State the preparation type.
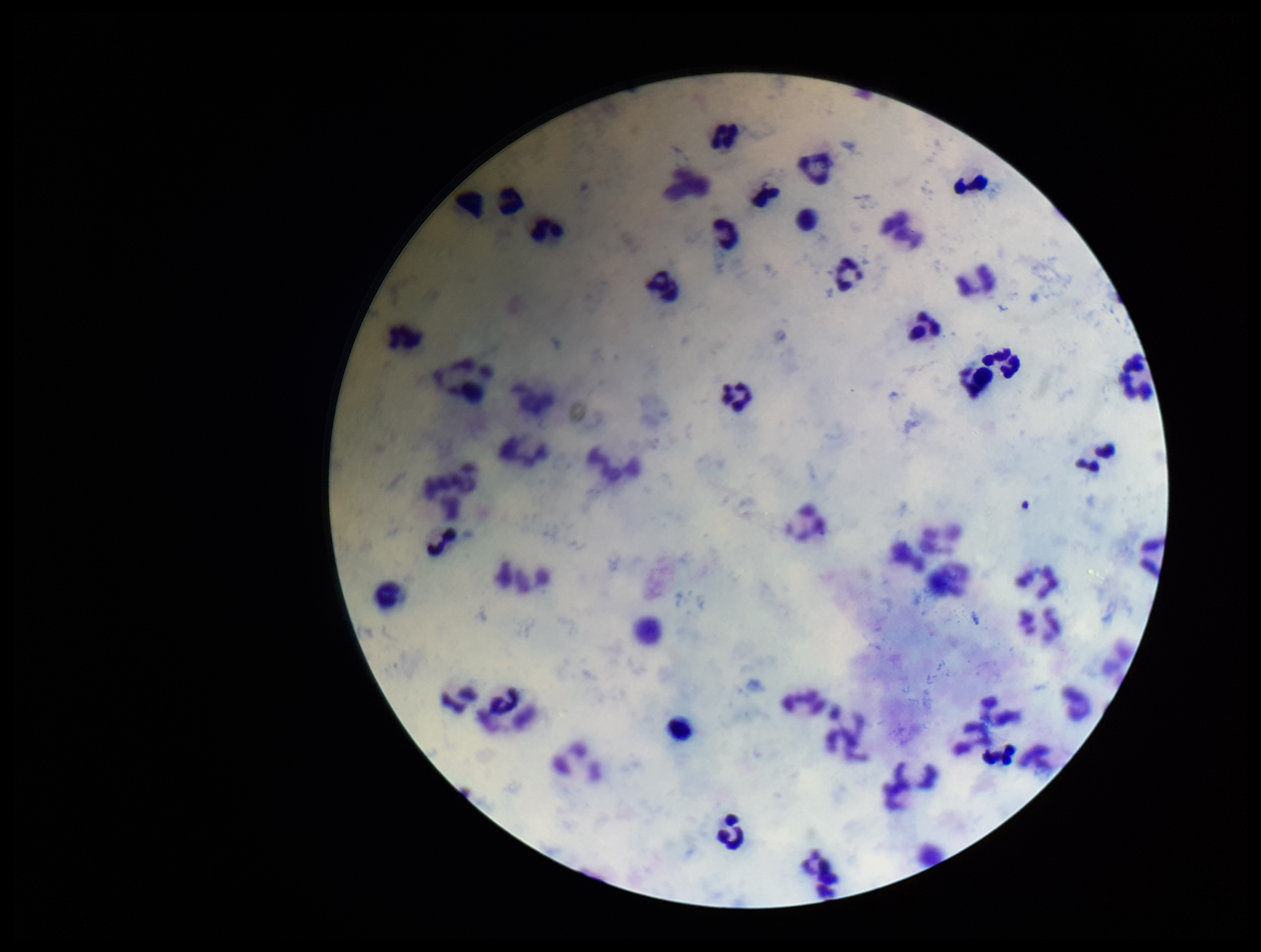

Thick.

Summary:
  - Image size: 1261×952 pixels
  - Leukocyte count: 54
  - Stain: Giemsa
  - Capture: smartphone photograph through the microscope eyepiece
  - Parasite count: 0
  - Patient malaria status: negative
  - Plasmodium parasites: none detected
  - Field of view: single